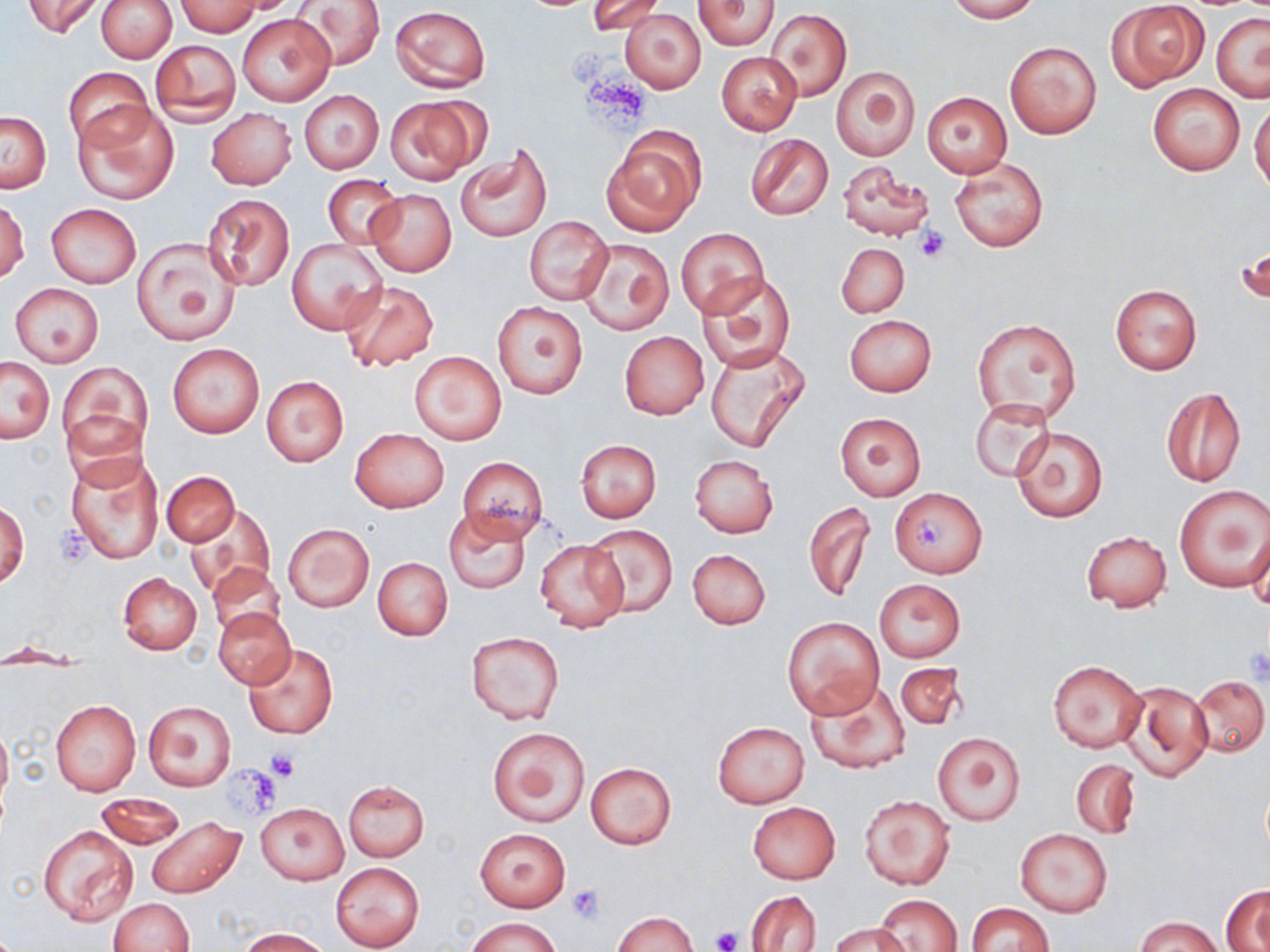
slide-level diagnosis = negative for blood parasites
uninfected red blood cell locations = approximate bounding boxes as [x1, y1, x2, y2] in pixels: [23, 0, 104, 39], [96, 0, 177, 63], [587, 0, 667, 37], [945, 0, 1039, 22], [293, 1, 386, 70], [692, 1, 780, 49], [177, 2, 258, 36], [1108, 2, 1207, 90], [391, 6, 489, 92], [765, 7, 850, 103], [621, 9, 708, 93], [238, 13, 337, 107], [1212, 13, 1270, 102], [150, 39, 240, 125], [1005, 40, 1101, 138], [717, 52, 801, 135], [831, 67, 919, 161], [63, 68, 152, 151], [1147, 83, 1245, 176], [300, 91, 384, 173], [922, 91, 1012, 178], [384, 95, 487, 184], [74, 103, 178, 204], [1250, 103, 1270, 192], [206, 108, 296, 189], [1, 110, 51, 192], [601, 129, 703, 236], [745, 134, 834, 221], [455, 148, 549, 242], [951, 158, 1048, 252], [837, 161, 933, 242], [323, 175, 403, 249], [367, 189, 456, 277], [201, 193, 295, 291], [1, 199, 30, 284], [46, 203, 142, 288], [524, 215, 614, 305], [676, 228, 769, 318], [131, 237, 240, 345], [578, 237, 674, 336], [287, 240, 387, 334], [1237, 242, 1268, 310], [836, 243, 909, 318], [698, 272, 795, 372], [339, 279, 439, 372], [10, 283, 104, 365], [1110, 283, 1201, 375], [493, 302, 588, 399], [844, 314, 937, 397], [972, 318, 1080, 422], [620, 332, 709, 419], [167, 342, 265, 439], [704, 344, 807, 452], [411, 351, 506, 445], [2, 356, 55, 443], [58, 361, 151, 458], [261, 376, 349, 467], [1161, 385, 1247, 487], [970, 399, 1054, 482], [834, 412, 925, 500], [1011, 427, 1109, 522], [351, 428, 449, 514], [575, 439, 661, 521], [67, 451, 162, 564], [690, 454, 778, 539], [459, 456, 549, 539], [161, 471, 238, 545], [1175, 486, 1269, 591], [890, 487, 987, 577], [1, 501, 29, 589], [803, 502, 875, 602], [187, 505, 276, 597], [443, 506, 533, 595], [1245, 520, 1270, 610], [283, 523, 373, 611], [585, 525, 679, 617], [1081, 530, 1172, 611], [534, 539, 628, 632], [688, 548, 770, 631], [372, 555, 453, 641], [207, 561, 287, 642], [118, 572, 202, 654], [875, 580, 965, 662], [213, 608, 296, 687], [782, 617, 885, 719], [464, 630, 566, 726], [242, 643, 339, 740], [1049, 659, 1147, 754], [894, 664, 967, 730], [1191, 675, 1269, 757], [1117, 679, 1213, 782], [806, 680, 911, 774], [51, 700, 140, 795], [144, 700, 236, 790], [713, 720, 809, 809], [0, 722, 12, 812], [486, 725, 590, 827], [932, 732, 1025, 826], [1071, 759, 1140, 838], [586, 762, 676, 849], [341, 780, 429, 861], [95, 792, 186, 850], [859, 794, 955, 890], [748, 802, 840, 883], [256, 803, 349, 884], [146, 817, 245, 899], [37, 825, 140, 927], [475, 828, 571, 911], [1016, 828, 1112, 916], [331, 863, 424, 950], [1221, 887, 1270, 951], [747, 890, 821, 951], [874, 894, 964, 952], [109, 898, 195, 951], [965, 903, 1054, 952], [612, 912, 698, 952], [1137, 916, 1221, 952], [467, 917, 561, 952], [829, 922, 910, 951], [239, 928, 330, 951]
preparation = thin blood film
stain = May-Grünwald-Giemsa
image size = 1270×952 pixels
platelet locations = approximate bounding boxes as [x1, y1, x2, y2] in pixels: [581, 73, 652, 129], [914, 225, 951, 262], [911, 515, 947, 555], [1244, 646, 1270, 685], [266, 748, 301, 782], [222, 766, 282, 819], [566, 884, 607, 923], [712, 926, 742, 952]
modality = optical microscopy
field of view = one of a larger specimen
magnification = 1000x